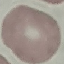 Malaria status: uninfected. Automatically extracted cell patch, resized to 64 × 64 pixels. Giemsa-stained preparation. Thin smear of blood. Photographed with a smartphone camera at the microscope eyepiece.